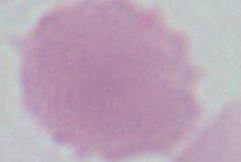

Photomicrograph. An erythrocyte is shown. 1000x magnification.